Identify the parasite.
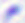
This is Toxoplasma gondii.

Photomicrograph. 400x magnification.